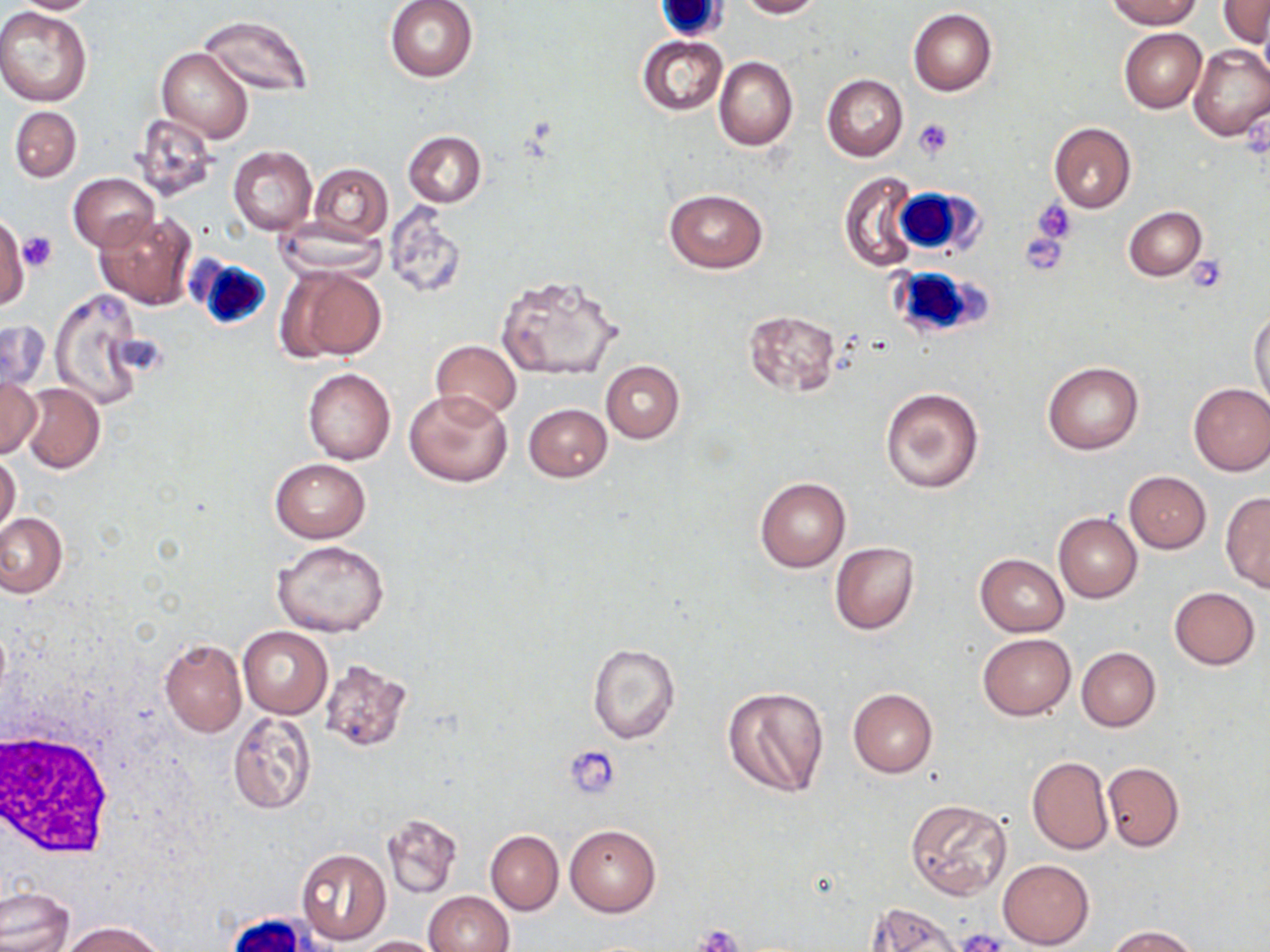

{
  "slide_level_diagnosis": "no evidence of blood parasites",
  "stain": "May-Grünwald-Giemsa",
  "modality": "light microscopy",
  "magnification": "1000x",
  "white_blood_cell_locations": "approximate bounding boxes as named x1/y1/x2/y2 corners in pixels: (x1=656, y1=0, x2=727, y2=38), (x1=890, y1=186, x2=977, y2=257), (x1=189, y1=255, x2=273, y2=332), (x1=887, y1=263, x2=987, y2=342), (x1=0, y1=729, x2=114, y2=857)",
  "platelet_locations": "approximate bounding boxes as named x1/y1/x2/y2 corners in pixels: (x1=912, y1=119, x2=956, y2=158), (x1=1033, y1=201, x2=1077, y2=243), (x1=1021, y1=230, x2=1069, y2=277), (x1=20, y1=231, x2=56, y2=272), (x1=1186, y1=257, x2=1230, y2=293), (x1=565, y1=747, x2=621, y2=797), (x1=695, y1=924, x2=744, y2=950), (x1=955, y1=929, x2=1007, y2=952)",
  "image_size": "1270×952 pixels",
  "uninfected_red_blood_cell_locations": "approximate bounding boxes as named x1/y1/x2/y2 corners in pixels: (x1=9, y1=0, x2=101, y2=14), (x1=384, y1=0, x2=478, y2=82), (x1=736, y1=0, x2=824, y2=18), (x1=1103, y1=0, x2=1203, y2=29), (x1=1218, y1=0, x2=1268, y2=47), (x1=0, y1=8, x2=93, y2=105), (x1=909, y1=9, x2=997, y2=95), (x1=198, y1=14, x2=313, y2=97), (x1=1119, y1=27, x2=1206, y2=113), (x1=637, y1=35, x2=729, y2=117), (x1=1188, y1=44, x2=1270, y2=142), (x1=157, y1=48, x2=253, y2=142), (x1=714, y1=56, x2=798, y2=150), (x1=822, y1=74, x2=908, y2=161), (x1=9, y1=104, x2=82, y2=183), (x1=130, y1=114, x2=220, y2=202), (x1=1049, y1=123, x2=1135, y2=213), (x1=403, y1=131, x2=487, y2=207), (x1=228, y1=146, x2=318, y2=234), (x1=309, y1=164, x2=392, y2=241), (x1=69, y1=172, x2=160, y2=252), (x1=839, y1=172, x2=920, y2=272), (x1=663, y1=188, x2=769, y2=274), (x1=383, y1=202, x2=466, y2=299), (x1=1122, y1=206, x2=1206, y2=280), (x1=95, y1=210, x2=196, y2=310), (x1=0, y1=214, x2=29, y2=311), (x1=272, y1=218, x2=387, y2=281), (x1=282, y1=266, x2=385, y2=360), (x1=496, y1=273, x2=624, y2=380), (x1=49, y1=288, x2=148, y2=410), (x1=1249, y1=307, x2=1270, y2=416), (x1=742, y1=309, x2=840, y2=396), (x1=0, y1=320, x2=50, y2=394), (x1=430, y1=339, x2=523, y2=421), (x1=601, y1=361, x2=684, y2=444), (x1=1042, y1=361, x2=1144, y2=455), (x1=302, y1=367, x2=395, y2=465), (x1=0, y1=374, x2=41, y2=459), (x1=1188, y1=382, x2=1270, y2=476), (x1=20, y1=383, x2=105, y2=473), (x1=880, y1=388, x2=984, y2=492), (x1=404, y1=389, x2=513, y2=488), (x1=524, y1=403, x2=611, y2=481), (x1=0, y1=452, x2=20, y2=535), (x1=271, y1=459, x2=370, y2=542), (x1=1124, y1=471, x2=1211, y2=553), (x1=755, y1=476, x2=850, y2=571), (x1=1221, y1=492, x2=1270, y2=592), (x1=0, y1=513, x2=66, y2=597), (x1=1053, y1=513, x2=1142, y2=603), (x1=273, y1=539, x2=390, y2=637), (x1=830, y1=542, x2=919, y2=635), (x1=975, y1=553, x2=1069, y2=636), (x1=1168, y1=587, x2=1260, y2=669), (x1=237, y1=626, x2=332, y2=718), (x1=978, y1=633, x2=1075, y2=720), (x1=158, y1=638, x2=246, y2=737), (x1=588, y1=644, x2=681, y2=745), (x1=1076, y1=647, x2=1160, y2=732), (x1=319, y1=658, x2=411, y2=751), (x1=721, y1=683, x2=829, y2=799), (x1=848, y1=688, x2=937, y2=777), (x1=228, y1=711, x2=317, y2=814), (x1=1026, y1=755, x2=1113, y2=855), (x1=1102, y1=761, x2=1184, y2=851), (x1=905, y1=799, x2=1012, y2=900), (x1=382, y1=815, x2=461, y2=898), (x1=564, y1=823, x2=661, y2=917), (x1=485, y1=829, x2=564, y2=915), (x1=295, y1=848, x2=392, y2=946), (x1=998, y1=859, x2=1094, y2=948), (x1=0, y1=886, x2=73, y2=952), (x1=424, y1=891, x2=514, y2=952), (x1=865, y1=902, x2=965, y2=952), (x1=66, y1=921, x2=161, y2=952), (x1=1106, y1=925, x2=1199, y2=952), (x1=359, y1=935, x2=446, y2=952)",
  "field_of_view": "one of a larger specimen",
  "preparation": "thin blood smear"
}